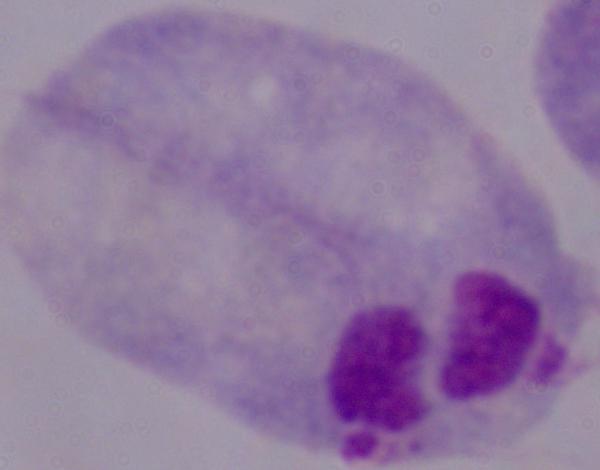 Micrograph. 1000x magnification. A trichomonad is shown.